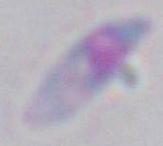

Captured at 1000x magnification. Photomicrograph. Toxoplasma gondii is seen.